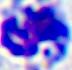

modality = micrograph
magnification = 400x
identification = leukocyte